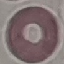

Malaria status: uninfected. Automatically extracted cell patch, resized to 64 × 64 pixels. Acquired by smartphone through the microscope eyepiece. Giemsa-stained preparation. Thin blood smear.